Name the parasite shown.
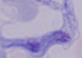

A trypanosome.

magnification = 1000x
modality = micrograph